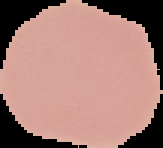

image size = 163×148 pixels
preparation = thin blood smear
image type = segmented cell region on a black background
result = no malaria parasites detected